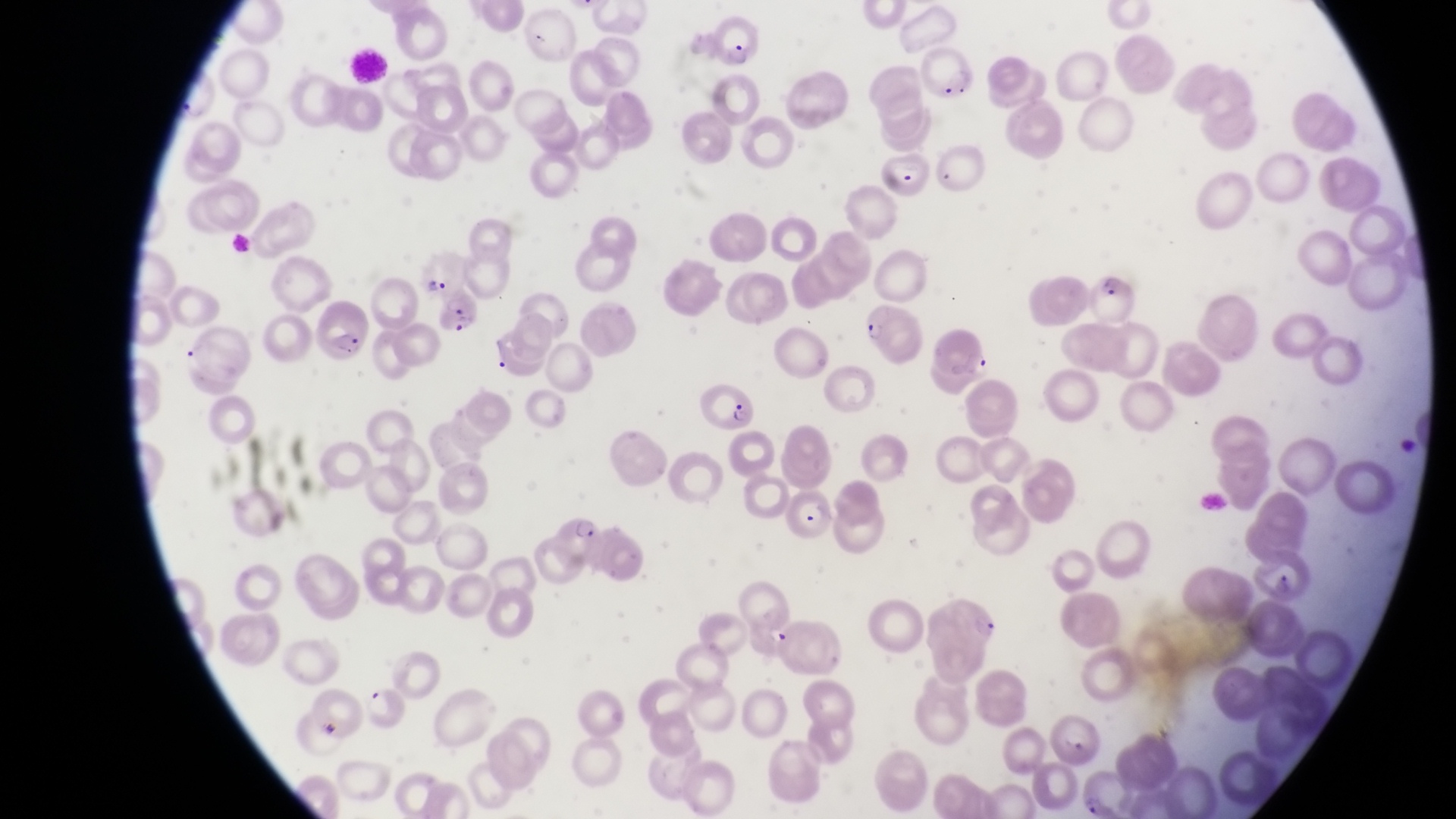
image size = 1456×819 pixels
field of view = single
capture = smartphone photograph through the eyepiece of an Olympus CX-23 microscope
magnification = 1000x
preparation = thin blood film
country = Uganda
parasitised red blood cell locations = approximate bounding boxes as [left, top, right, bottom] in pixels: [713, 13, 759, 69], [917, 43, 977, 98], [880, 148, 940, 197], [1090, 270, 1140, 328], [438, 291, 483, 337], [858, 300, 924, 366], [323, 304, 369, 360], [700, 378, 756, 436], [792, 485, 837, 548], [558, 510, 613, 569]